Give the position of every leukocyte visible.
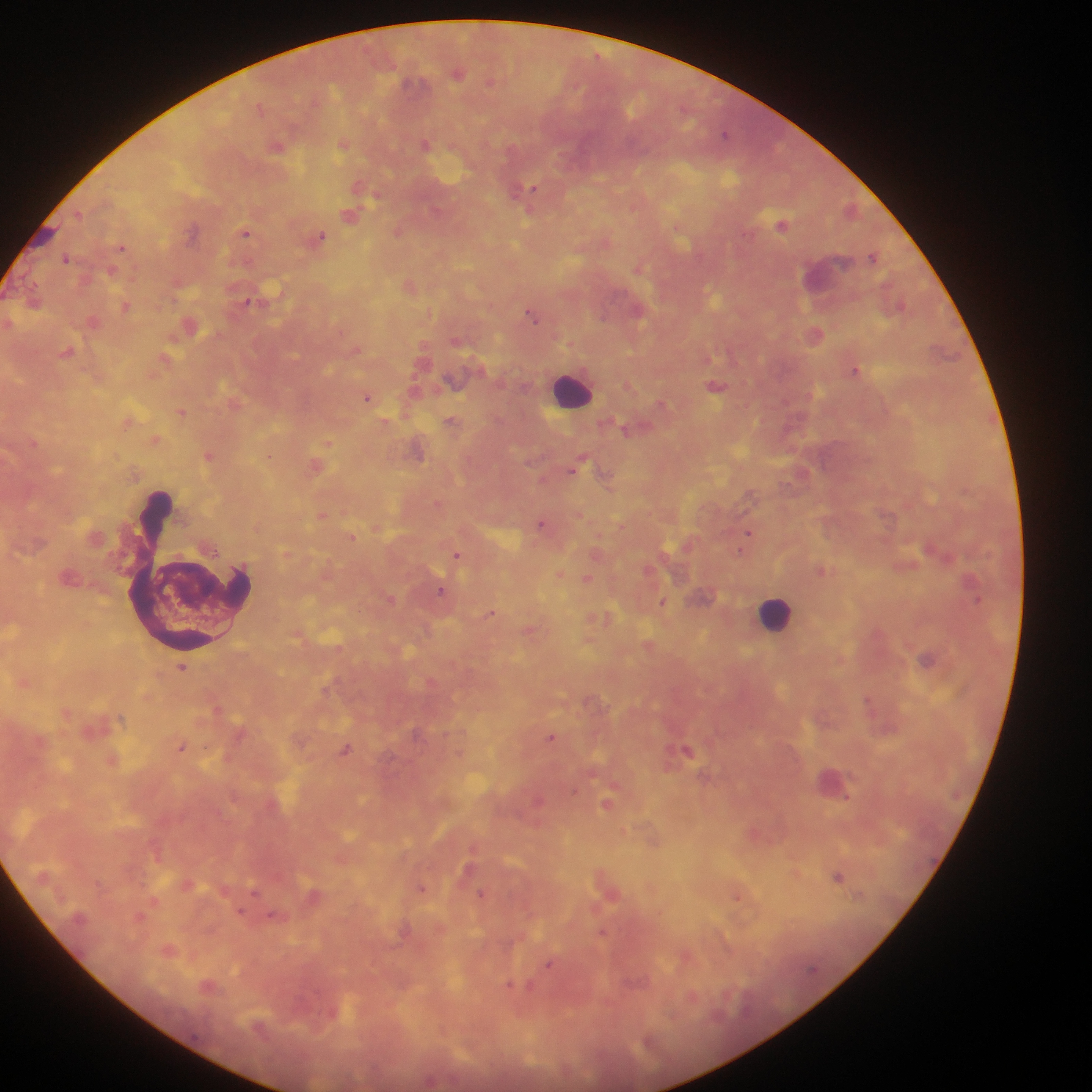
Approximate centers as {x, y} in pixels.
Leukocytes: {571, 388}, {192, 569}, {777, 614}.

Malaria parasite locations: {458, 72}, {491, 81}, {259, 107}, {725, 133}, {424, 144}, {343, 145}, {277, 147}, {528, 189}, {349, 216}, {782, 226}, {397, 230}, {246, 233}, {321, 235}, {122, 247}, {873, 256}, {66, 258}, {638, 267}, {247, 301}, {900, 304}, {126, 307}, {531, 314}, {816, 334}, {855, 370}, {716, 386}, {367, 397}, {661, 403}, {182, 412}, {450, 421}, {624, 429}, {34, 444}, {328, 444}, {209, 456}, {269, 456}, {575, 467}, {605, 476}, {750, 496}, {541, 523}, {748, 534}, {352, 537}, {744, 544}, {929, 549}, {456, 554}, {587, 578}, {441, 590}, {390, 598}, {977, 600}, {662, 603}, {491, 613}, {927, 659}, {182, 667}, {867, 699}, {551, 737}, {182, 746}, {346, 749}, {688, 750}, {846, 798}, {607, 804}, {838, 876}, {421, 888}, {254, 891}, {481, 893}, {738, 897}, {271, 916}, {602, 932}, {548, 965}, {518, 987}. Photographed through a microscope with a mobile-phone camera. One field of view. Image is 1092×1092 pixels. Sample from Ghana. Thick blood smear.